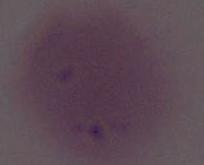

Summary:
  - Magnification: 1000x
  - Identification: erythrocyte
  - Modality: micrograph